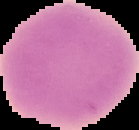

image type = segmented cell region with the area outside set to black
result = no Plasmodium parasites seen
image size = 139×130 pixels
preparation = thin blood smear